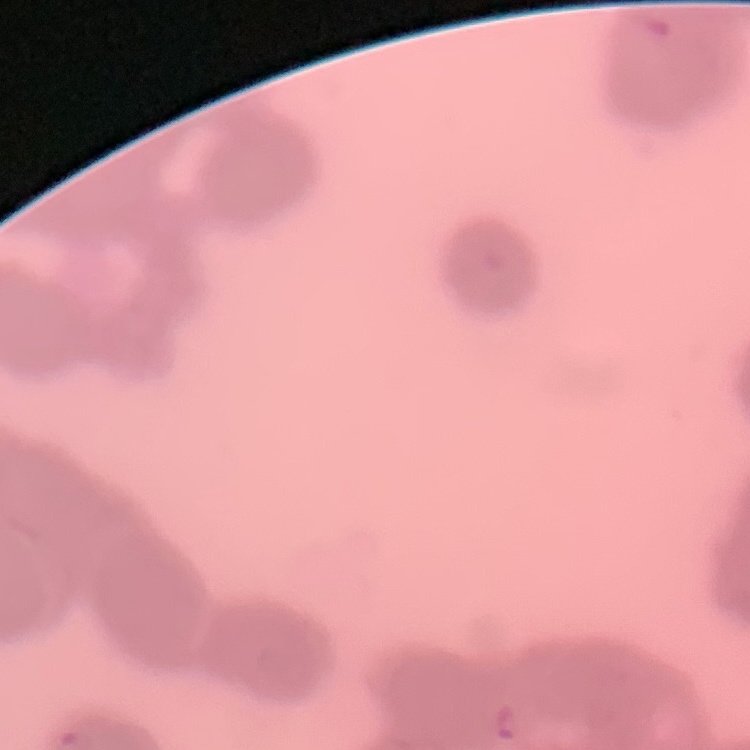

Summary:
  - Erythrocyte morphology: rouleaux formation
  - Image type: one tile cut from a larger photomicrograph
  - Stain: Field's or Giemsa
  - Preparation: thin blood smear